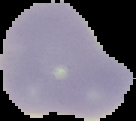

{
  "image_size": "136×121 pixels",
  "image_type": "segmented cell region on a black background",
  "preparation": "thin blood film",
  "result": "no malaria parasites detected"
}